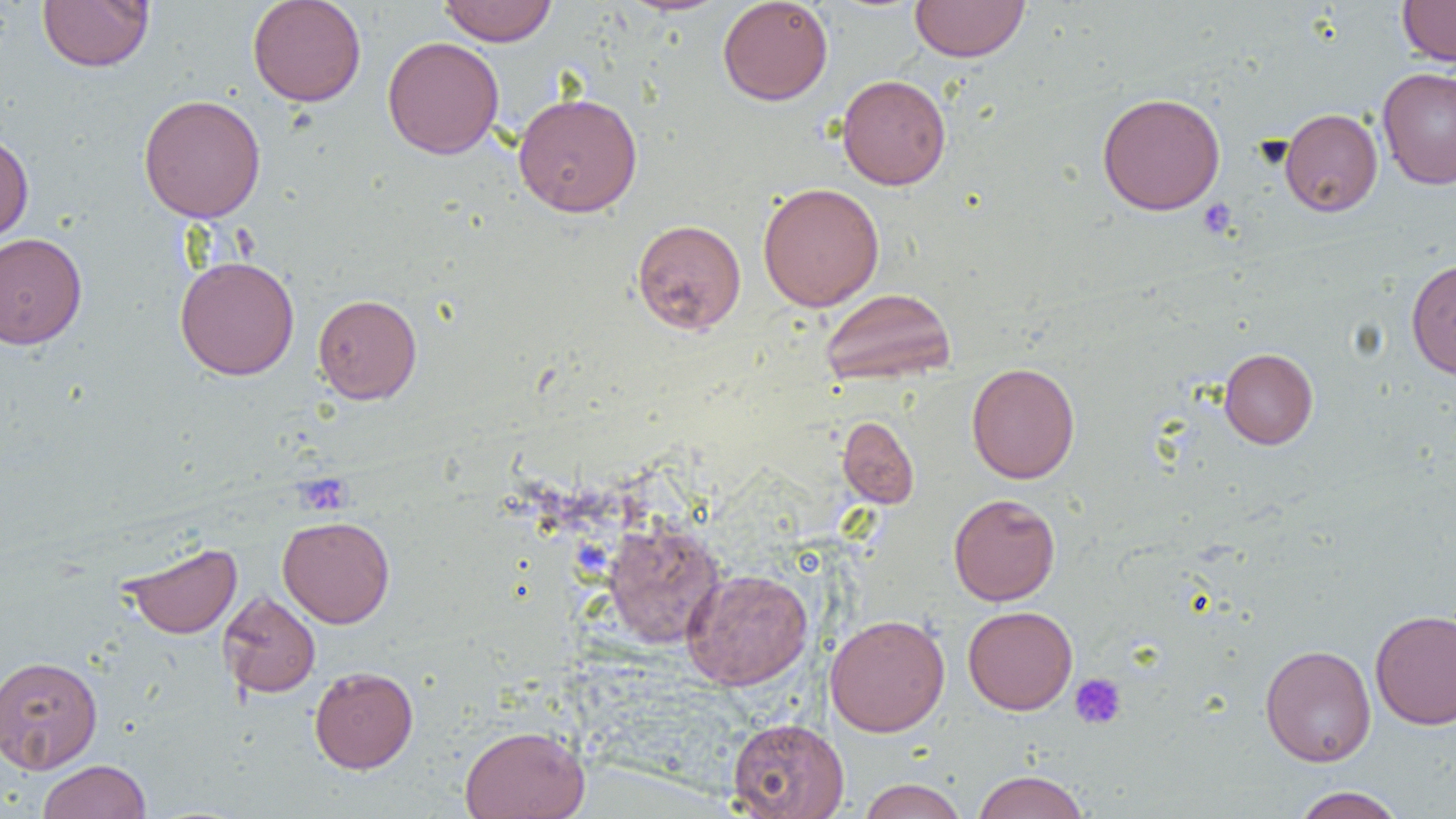
slide_level_diagnosis: no evidence of blood parasites
magnification: 1000x
uninfected_red_blood_cell_locations: 'approximate bounding boxes as named x1/y1/x2/y2 corners in pixels: (x1=37, y1=0, x2=155, y2=72), (x1=247, y1=0, x2=366, y2=107), (x1=438, y1=0, x2=558, y2=46), (x1=618, y1=0, x2=732, y2=16), (x1=717, y1=0, x2=833, y2=105), (x1=909, y1=0, x2=1030, y2=62), (x1=1398, y1=0, x2=1456, y2=66), (x1=382, y1=36, x2=505, y2=159), (x1=1377, y1=67, x2=1456, y2=191), (x1=836, y1=74, x2=951, y2=190), (x1=513, y1=92, x2=643, y2=217), (x1=1097, y1=92, x2=1225, y2=215), (x1=138, y1=94, x2=266, y2=223), (x1=1279, y1=108, x2=1383, y2=217), (x1=0, y1=133, x2=34, y2=242), (x1=757, y1=182, x2=885, y2=312), (x1=631, y1=218, x2=746, y2=335), (x1=0, y1=232, x2=87, y2=349), (x1=174, y1=255, x2=300, y2=380), (x1=1405, y1=258, x2=1456, y2=379), (x1=820, y1=287, x2=956, y2=385), (x1=312, y1=293, x2=422, y2=405), (x1=1218, y1=348, x2=1318, y2=449), (x1=966, y1=362, x2=1080, y2=484), (x1=837, y1=415, x2=919, y2=508), (x1=948, y1=493, x2=1061, y2=606), (x1=277, y1=515, x2=395, y2=628), (x1=602, y1=518, x2=727, y2=648), (x1=119, y1=541, x2=243, y2=639), (x1=682, y1=568, x2=814, y2=690), (x1=217, y1=591, x2=321, y2=699), (x1=963, y1=605, x2=1077, y2=714), (x1=1370, y1=608, x2=1456, y2=730), (x1=825, y1=614, x2=950, y2=736), (x1=1260, y1=644, x2=1376, y2=767), (x1=0, y1=655, x2=103, y2=774), (x1=309, y1=665, x2=418, y2=773), (x1=727, y1=717, x2=850, y2=818), (x1=459, y1=724, x2=589, y2=819), (x1=38, y1=759, x2=151, y2=819), (x1=971, y1=770, x2=1089, y2=819), (x1=858, y1=778, x2=967, y2=819), (x1=1291, y1=786, x2=1406, y2=819)'
preparation: thin blood film
modality: optical microscopy
field_of_view: single
image_size: 1456×819 pixels
platelet_locations: 'approximate bounding boxes as named x1/y1/x2/y2 corners in pixels: (x1=1197, y1=198, x2=1237, y2=238), (x1=295, y1=474, x2=354, y2=516), (x1=1070, y1=672, x2=1127, y2=730)'